Classify this cell by malaria status.
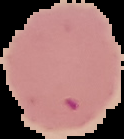
Parasitized.

Summary:
  - Image size: 124×139 pixels
  - Image type: cell region segmented out of the field of view; surrounding area masked to black
  - Preparation: thin blood smear